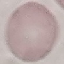

Summary:
  - Malaria status: uninfected
  - Image type: automatically extracted cell patch, resized to 64 × 64 pixels
  - Capture: smartphone camera at the microscope eyepiece
  - Preparation: thin smear
  - Stain: Giemsa